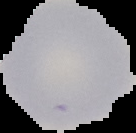
Segmented cell region on a black background. From a thin blood smear. Image is 136×133 pixels. Malaria status: uninfected.